Give the position of every leukocyte visible.
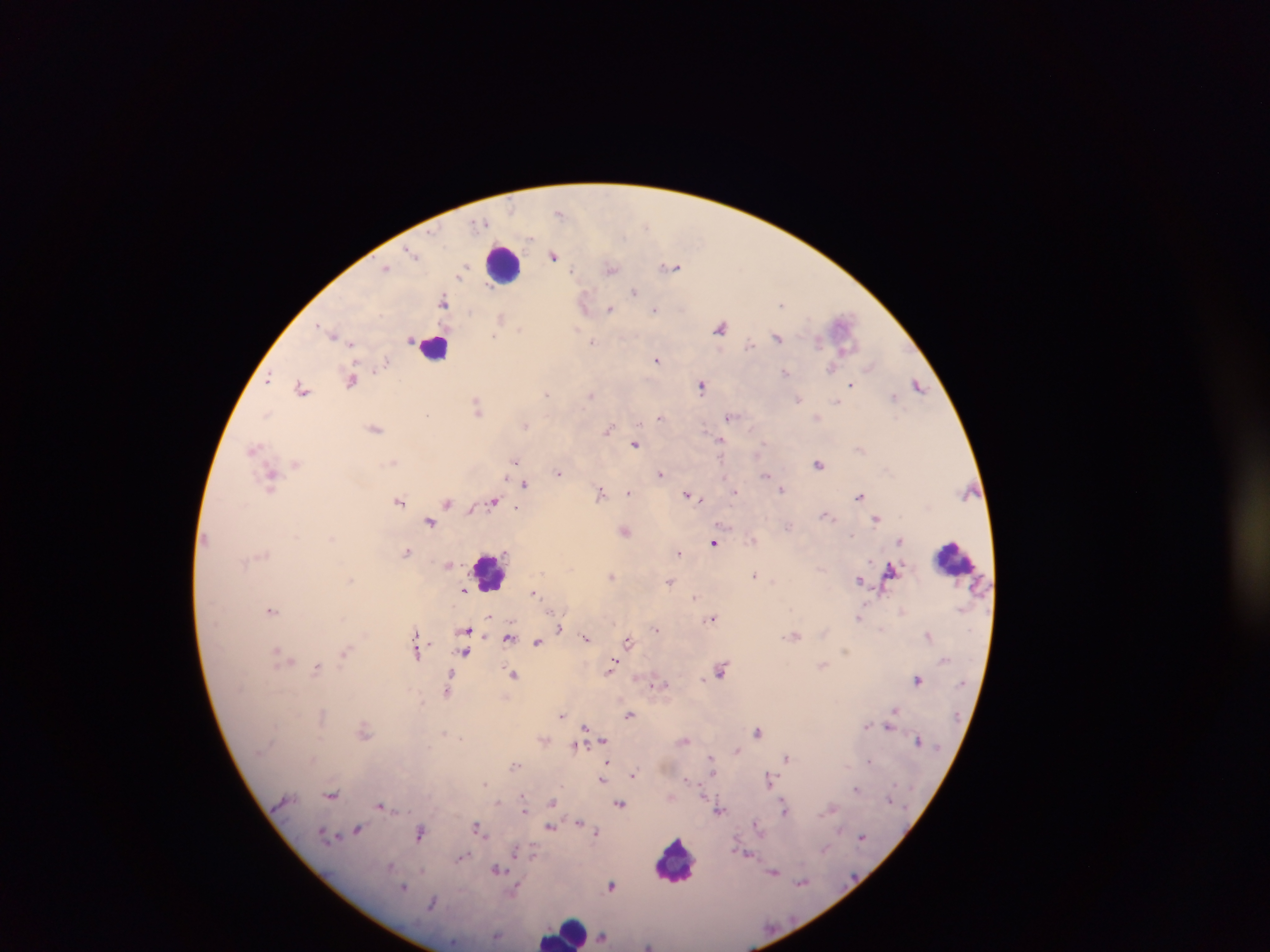

Approximate centers as (x, y) in pixels.
Leukocytes: (502, 263), (435, 347), (954, 558), (489, 572), (676, 862), (565, 932).

{
  "preparation": "thick blood film",
  "field_of_view": "single",
  "capture": "mobile-phone photograph through a microscope",
  "plasmodium_parasite_locations": "approximate centers as (x, y) in pixels: (561, 211), (553, 255), (672, 266), (387, 267), (611, 269), (635, 291), (444, 301), (585, 304), (781, 304), (609, 308), (655, 309), (502, 318), (842, 326), (721, 327), (520, 328), (332, 333), (778, 337), (410, 338), (594, 341), (751, 345), (657, 358), (871, 366), (831, 368), (786, 373), (353, 378), (268, 379), (701, 384), (851, 385), (918, 385), (303, 387), (547, 393), (591, 394), (894, 396), (798, 398), (837, 402), (477, 406), (266, 414), (426, 414), (730, 416), (661, 417), (817, 417), (525, 424), (375, 428), (609, 429), (721, 440), (636, 443), (861, 447), (254, 448), (514, 460), (297, 463), (394, 463), (819, 463), (558, 472), (661, 474), (765, 474), (273, 478), (524, 483), (782, 489), (601, 491), (735, 491), (629, 492), (688, 494), (859, 495), (699, 498), (399, 501), (448, 501), (494, 501), (518, 507), (473, 508), (826, 515), (877, 517), (431, 522), (624, 530), (901, 541), (715, 542), (407, 551), (678, 553), (450, 564), (892, 568), (755, 574), (612, 575), (860, 580), (670, 581), (464, 589), (534, 592), (696, 597), (271, 610), (902, 611), (490, 616), (712, 617), (860, 617), (560, 629), (656, 629), (466, 630), (417, 635), (467, 635), (795, 635), (929, 635), (509, 636), (587, 637), (539, 640), (629, 640), (418, 650), (467, 650), (278, 652), (345, 652), (284, 659), (823, 664), (317, 667), (612, 667), (721, 669), (513, 673), (450, 678), (918, 678), (658, 683), (448, 691), (894, 710), (562, 714), (631, 714), (892, 715), (891, 724), (586, 726), (867, 726), (363, 729), (759, 731), (544, 740), (603, 740), (685, 740), (918, 740), (577, 745), (736, 749), (787, 758), (711, 759), (607, 764), (515, 765), (633, 774), (769, 779), (603, 780), (688, 780), (485, 783), (857, 789), (332, 794), (704, 796), (524, 800), (621, 802), (498, 803), (553, 803), (381, 805), (785, 808), (832, 808), (526, 809), (720, 810), (579, 821), (757, 824), (551, 826), (478, 828), (358, 829), (597, 831), (420, 832), (862, 836), (825, 849), (515, 851), (745, 853), (464, 856), (496, 868), (774, 871), (802, 882), (612, 885), (404, 886), (516, 889), (497, 936), (604, 937), (648, 945)",
  "country": "Ghana",
  "image_size": "1270×952 pixels"
}